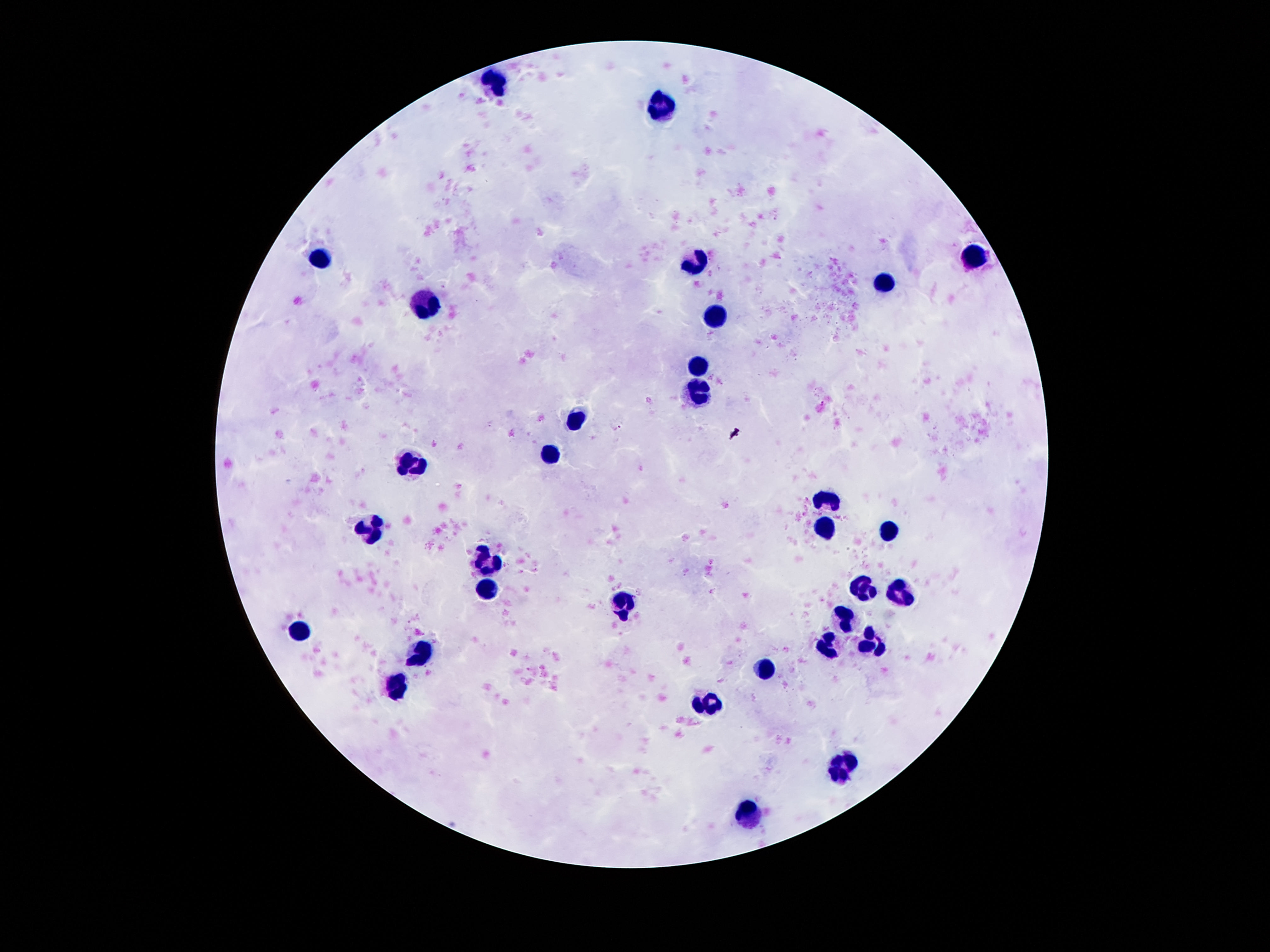

Approximate centers as [x, y] in pixels.
Summary:
  - Leukocyte locations: [494, 81], [659, 103], [977, 256], [318, 260], [695, 263], [884, 284], [424, 306], [714, 316], [700, 368], [697, 390], [575, 419], [548, 457], [410, 466], [828, 501], [369, 529], [822, 529], [890, 531], [486, 561], [860, 585], [489, 588], [898, 594], [624, 605], [844, 619], [299, 629], [871, 640], [825, 643], [424, 647], [762, 670], [397, 683], [711, 702], [844, 769], [749, 811]
  - Preparation: thick blood smear
  - Image size: 1270×952 pixels
  - Capture: smartphone camera through the microscope eyepiece
  - Field of view: one from this slide
  - Stain: Giemsa
  - Magnification: 100x
  - Patient malaria status: uninfected